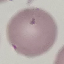
Summary:
  - Result: negative for malaria parasites
  - Stain: Giemsa
  - Capture: smartphone through the microscope eyepiece
  - Image type: cell patch, automatically extracted from a larger field of view and resized to 64 × 64 pixels
  - Preparation: thin blood smear